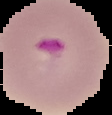
preparation = thin blood film
result = malaria parasites identified
image size = 112×115 pixels
image type = segmented cell region on a black background